Point out each leukocyte.
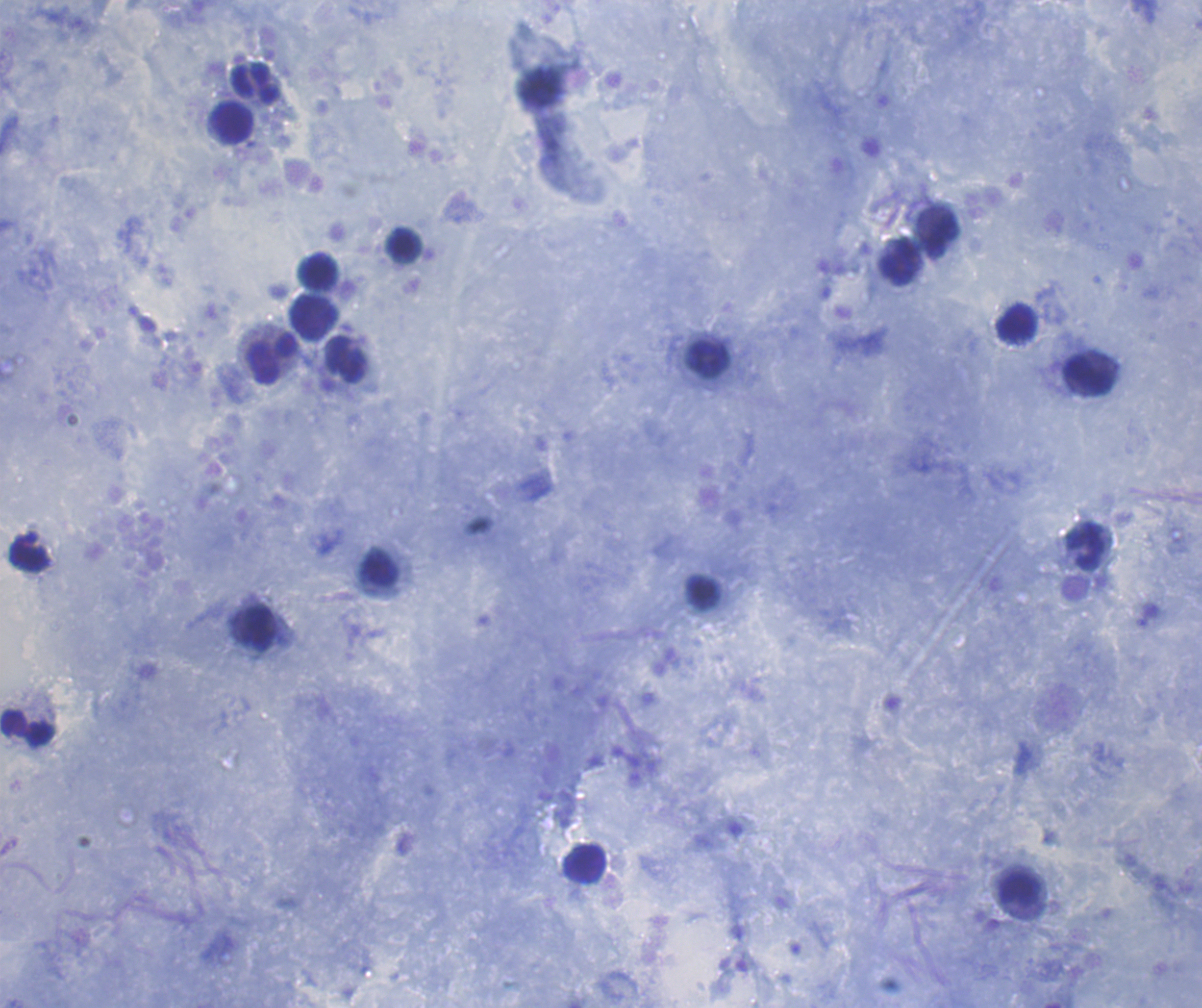

Approximate centers as (x, y) in pixels.
Leukocytes: (257, 83), (232, 122), (942, 235), (404, 245), (900, 262), (318, 270), (314, 316), (1016, 322), (272, 358), (707, 359), (346, 361), (1088, 376), (1086, 547), (30, 557), (379, 567), (704, 593), (255, 627), (27, 726), (584, 863), (1020, 890).

Summary:
  - Result: no malaria parasites seen
  - Stain: Romanowsky
  - Image size: 1202×1008 pixels
  - Coloration quality: good
  - Field of view: one from this slide
  - Preparation: thick blood smear
  - Context: previously used in a real diagnosis
  - Background quality: satisfactory
  - Magnification: 100x